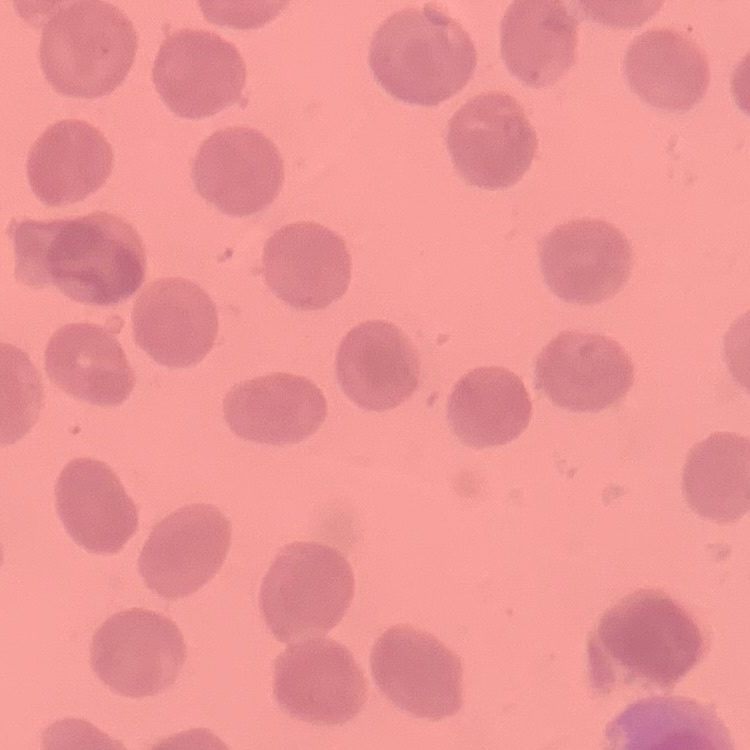

erythrocyte_morphology: no rouleaux formation
image_type: square crop of a larger photomicrograph
stain: Field's or Giemsa
preparation: thin blood film